Assess the morphology of the red blood cells.
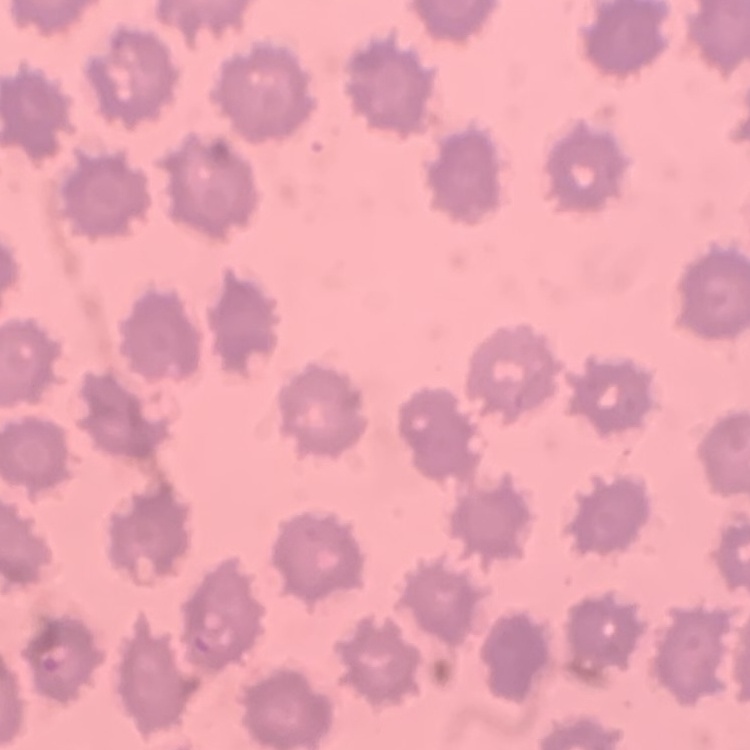
They show no rouleaux formation.

preparation = thin blood smear
stain = Field's or Giemsa
image type = square crop of a larger photomicrograph